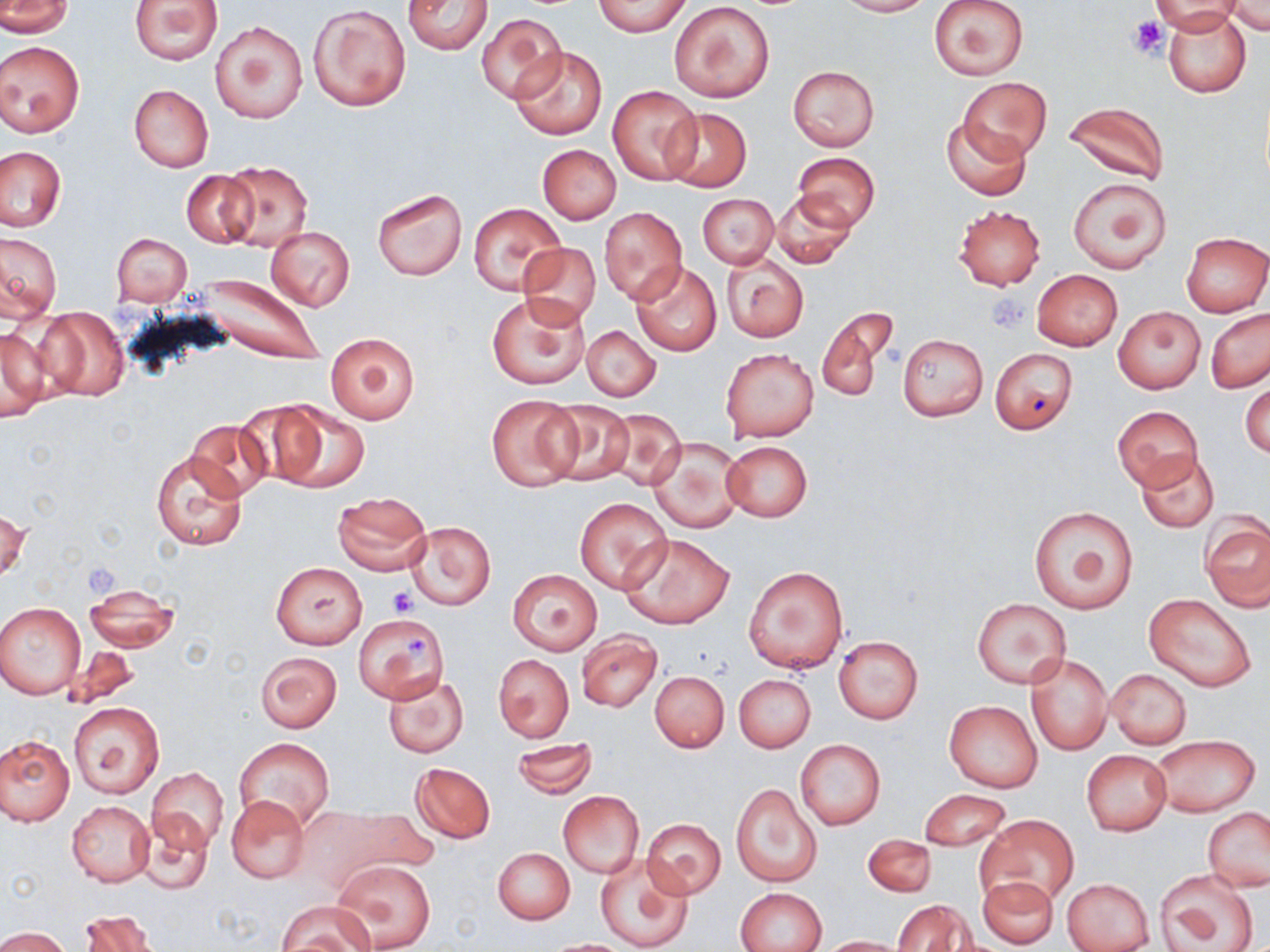

slide-level diagnosis = no evidence of blood parasites
platelet locations = approximate bounding boxes as (x1,y1)-(x2,y2) corner pairs in pixels: (1129,16)-(1167,59), (988,293)-(1030,333), (388,586)-(416,616), (405,632)-(432,660)
preparation = thin blood film
magnification = 1000x
field of view = single
modality = light microscopy
uninfected red blood cell locations = approximate bounding boxes as (x1,y1)-(x2,y2) corner pairs in pixels: (5,0)-(72,37), (129,0)-(223,65), (402,0)-(493,54), (834,0)-(931,16), (929,0)-(1029,81), (1152,0)-(1243,33), (592,1)-(692,36), (1224,1)-(1269,33), (670,2)-(775,102), (308,3)-(411,111), (1163,8)-(1251,98), (476,11)-(567,104), (210,19)-(308,124), (0,41)-(85,137), (511,46)-(607,140), (787,65)-(880,151), (961,77)-(1050,160), (129,84)-(213,171), (607,84)-(701,184), (1063,101)-(1169,184), (662,106)-(751,192), (942,117)-(1030,201), (537,145)-(620,224), (1,147)-(65,231), (791,152)-(881,230), (221,161)-(313,251), (181,171)-(258,249), (1068,178)-(1171,274), (372,187)-(467,280), (767,190)-(857,268), (697,193)-(779,269), (469,203)-(564,294), (953,205)-(1046,290), (600,207)-(687,303), (265,226)-(356,311), (0,231)-(62,321), (111,231)-(191,306), (1181,232)-(1268,317), (517,242)-(600,328), (721,253)-(809,342), (629,260)-(723,356), (1031,269)-(1123,352), (176,271)-(331,367), (487,292)-(591,390), (34,306)-(128,403), (816,307)-(897,403), (1113,307)-(1205,392), (1205,309)-(1270,393), (582,324)-(661,402), (0,325)-(52,422), (325,334)-(420,424), (897,334)-(988,421), (720,347)-(820,441), (988,347)-(1078,434), (1241,375)-(1269,461), (486,395)-(582,492), (537,399)-(636,488), (268,400)-(371,494), (1113,405)-(1202,491), (600,408)-(689,492), (185,419)-(273,502), (647,436)-(744,535), (721,441)-(813,522), (151,450)-(249,551), (1135,450)-(1219,533), (332,492)-(432,576), (574,497)-(672,594), (1029,506)-(1138,613), (1,508)-(30,584), (1201,516)-(1270,611), (405,521)-(495,610), (619,533)-(733,630), (271,562)-(366,649), (744,566)-(849,673), (508,569)-(603,655), (83,585)-(182,652), (1145,593)-(1256,692), (972,598)-(1072,688), (0,602)-(86,699), (353,611)-(449,702), (576,630)-(663,711), (833,636)-(922,724), (254,650)-(343,733), (493,653)-(574,743), (1025,653)-(1112,755), (1105,669)-(1191,749), (650,671)-(729,753), (383,674)-(470,758), (734,674)-(816,753), (944,700)-(1042,793), (68,701)-(163,798), (1149,734)-(1259,817), (0,735)-(73,826), (234,738)-(334,832), (510,738)-(598,798), (795,739)-(885,830), (1082,750)-(1171,835), (409,762)-(495,844), (148,768)-(228,850), (729,782)-(821,888), (557,790)-(645,880), (919,790)-(1011,850), (226,796)-(309,884), (67,800)-(154,887), (290,803)-(434,897), (1203,808)-(1270,892), (135,812)-(213,895), (976,814)-(1076,908), (639,818)-(726,898), (862,834)-(936,897), (493,848)-(575,924), (594,852)-(694,951), (334,859)-(436,951), (1155,869)-(1261,950), (979,875)-(1058,948), (1062,877)-(1154,952), (736,888)-(826,952), (275,899)-(376,951), (894,899)-(975,952), (79,909)-(158,952), (0,927)-(71,952), (817,936)-(911,951), (543,939)-(636,951)
image size = 1270×952 pixels
stain = May-Grünwald-Giemsa